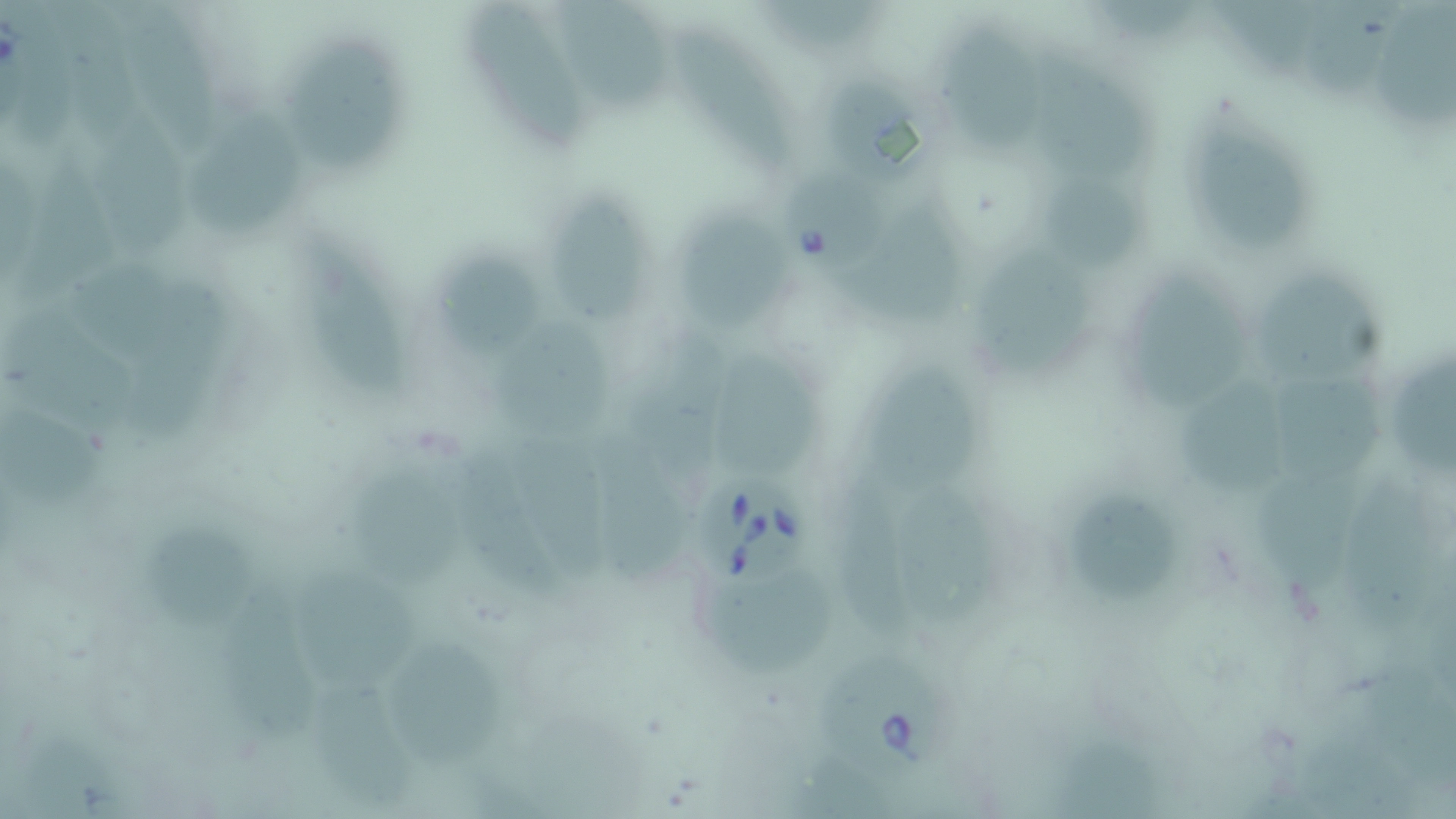

Approximate bounding boxes as [x1, y1, x2, y2] in pixels. Uninfected red blood cell locations: [558, 0, 673, 117], [1106, 0, 1213, 50], [1225, 2, 1331, 84], [761, 3, 897, 53], [1377, 3, 1455, 128], [9, 6, 83, 148], [125, 7, 222, 152], [58, 9, 147, 143], [1308, 9, 1404, 96], [469, 15, 593, 147], [678, 27, 803, 168], [945, 29, 1042, 159], [1035, 47, 1161, 182], [295, 49, 416, 178], [824, 74, 917, 176], [193, 97, 303, 239], [1192, 125, 1308, 255], [102, 129, 192, 251], [24, 151, 122, 294], [1054, 173, 1145, 274], [564, 194, 658, 326], [677, 202, 800, 328], [855, 206, 975, 340], [308, 232, 406, 401], [448, 243, 554, 365], [989, 254, 1091, 368], [1134, 258, 1240, 406], [78, 265, 193, 367], [1262, 277, 1381, 383], [1, 302, 139, 439], [505, 317, 607, 440], [641, 330, 737, 483], [1392, 356, 1456, 483], [721, 357, 823, 483], [874, 371, 995, 499], [1181, 373, 1291, 495], [1276, 373, 1388, 489], [1, 407, 102, 509], [464, 438, 558, 607], [523, 438, 611, 581], [593, 440, 689, 584], [346, 464, 475, 592], [843, 480, 926, 640], [1262, 480, 1354, 597], [1343, 483, 1428, 632], [1083, 490, 1182, 603], [917, 494, 992, 624], [147, 525, 261, 633], [300, 565, 421, 691], [711, 576, 842, 676], [210, 577, 330, 750], [401, 631, 516, 762], [1371, 664, 1455, 785], [311, 672, 418, 808], [1056, 726, 1160, 816], [1303, 726, 1416, 819], [796, 766, 879, 819]. Babesia divergens-infected red blood cell locations: [784, 169, 889, 281], [698, 478, 815, 585], [818, 649, 967, 780]. Slide-level diagnosis: Babesia divergens. May-Grünwald-Giemsa-stained preparation. Captured at 1000x magnification. Image is 1456×819 pixels. Light microscopy. Thin blood film. Single field of view.